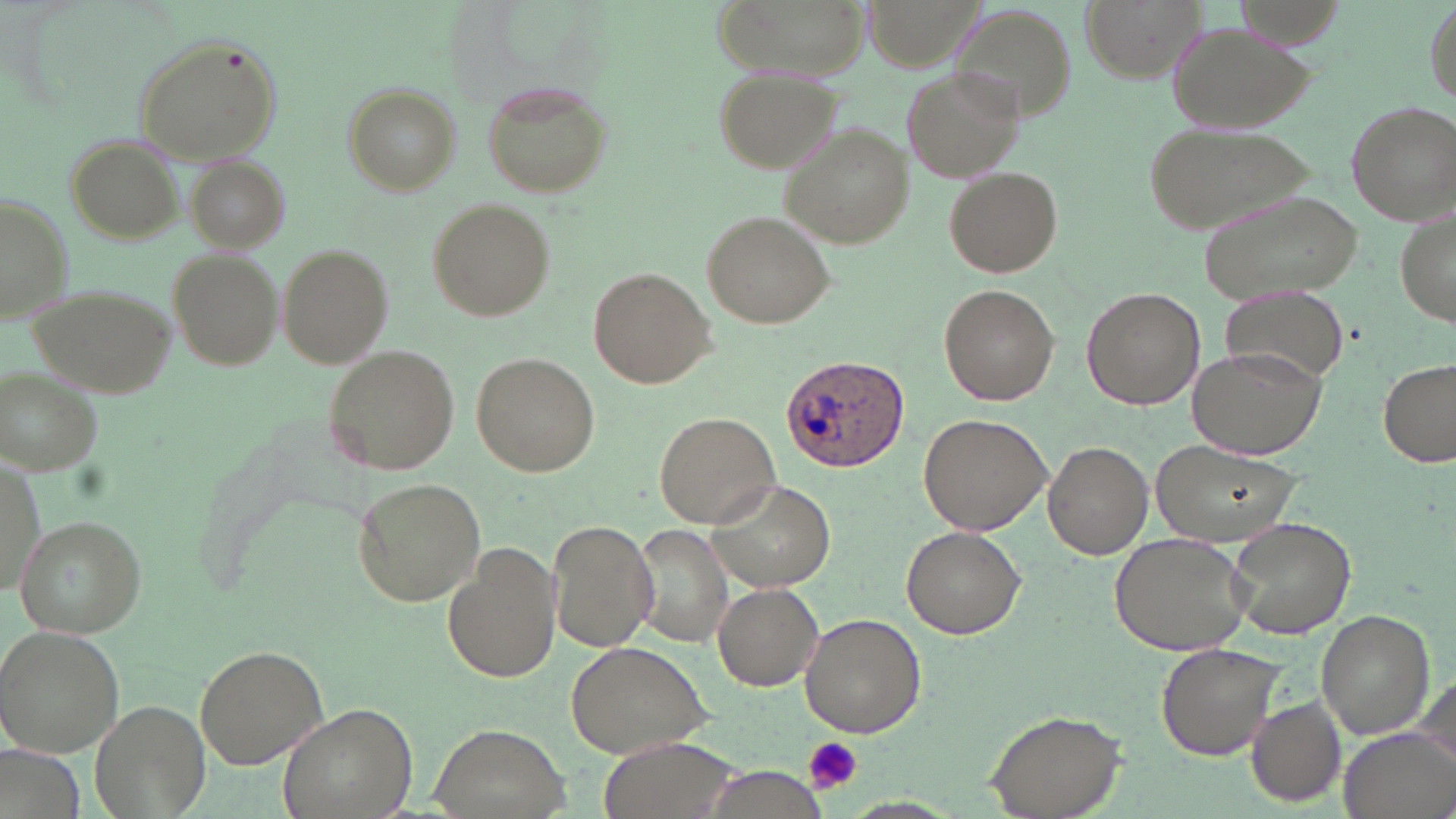
slide_level_diagnosis: Plasmodium ovale
field_of_view: single
platelet_locations: 'approximate bounding boxes as (x1, y1, x2, y2) in pixels: (804, 735, 861, 795)'
image_size: 1456×819 pixels
stain: May-Grünwald-Giemsa
magnification: 1000x
modality: light microscopy
plasmodium_ovale_infected_red_blood_cell_locations: 'approximate bounding boxes as (x1, y1, x2, y2) in pixels: (780, 355, 911, 473)'
uninfected_red_blood_cell_locations: 'approximate bounding boxes as (x1, y1, x2, y2) in pixels: (709, 0, 871, 78), (1082, 0, 1205, 80), (944, 6, 1081, 130), (1166, 18, 1317, 135), (130, 35, 283, 165), (901, 66, 1023, 185), (713, 70, 838, 176), (484, 82, 611, 196), (345, 85, 458, 195), (1344, 96, 1456, 223), (1142, 122, 1319, 233), (784, 125, 914, 249), (65, 133, 182, 246), (186, 156, 288, 253), (945, 167, 1063, 277), (1198, 187, 1362, 303), (1, 194, 73, 324), (427, 198, 553, 320), (1395, 203, 1455, 328), (702, 210, 836, 330), (280, 245, 392, 367), (170, 248, 284, 370), (589, 266, 714, 389), (27, 283, 177, 398), (939, 284, 1058, 404), (1082, 285, 1204, 409), (1218, 286, 1352, 389), (1189, 344, 1327, 458), (325, 346, 461, 475), (472, 353, 599, 477), (1378, 357, 1454, 468), (1, 370, 103, 475), (654, 411, 780, 527), (919, 413, 1052, 537), (1153, 438, 1302, 545), (1043, 440, 1153, 560), (2, 456, 43, 598), (352, 477, 483, 607), (706, 478, 838, 592), (16, 516, 145, 638), (1226, 516, 1358, 642), (547, 520, 658, 653), (631, 525, 734, 645), (902, 525, 1028, 638), (1107, 531, 1254, 656), (444, 543, 560, 685), (713, 584, 824, 690), (1316, 611, 1433, 738), (800, 613, 926, 736), (0, 627, 122, 757), (564, 641, 714, 761), (196, 643, 332, 770), (1156, 643, 1286, 762), (1412, 674, 1455, 772), (1246, 696, 1347, 805), (92, 700, 210, 819), (279, 701, 417, 819), (984, 709, 1125, 818), (432, 726, 571, 819), (1338, 726, 1456, 819), (598, 735, 742, 819), (701, 764, 834, 819)'
preparation: thin blood smear